Identify the parasite.
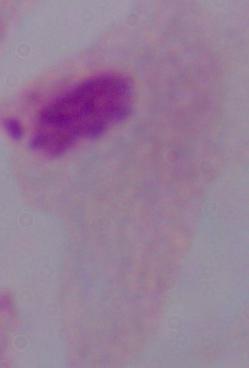
A trichomonad.

{
  "magnification": "1000x",
  "modality": "micrograph"
}